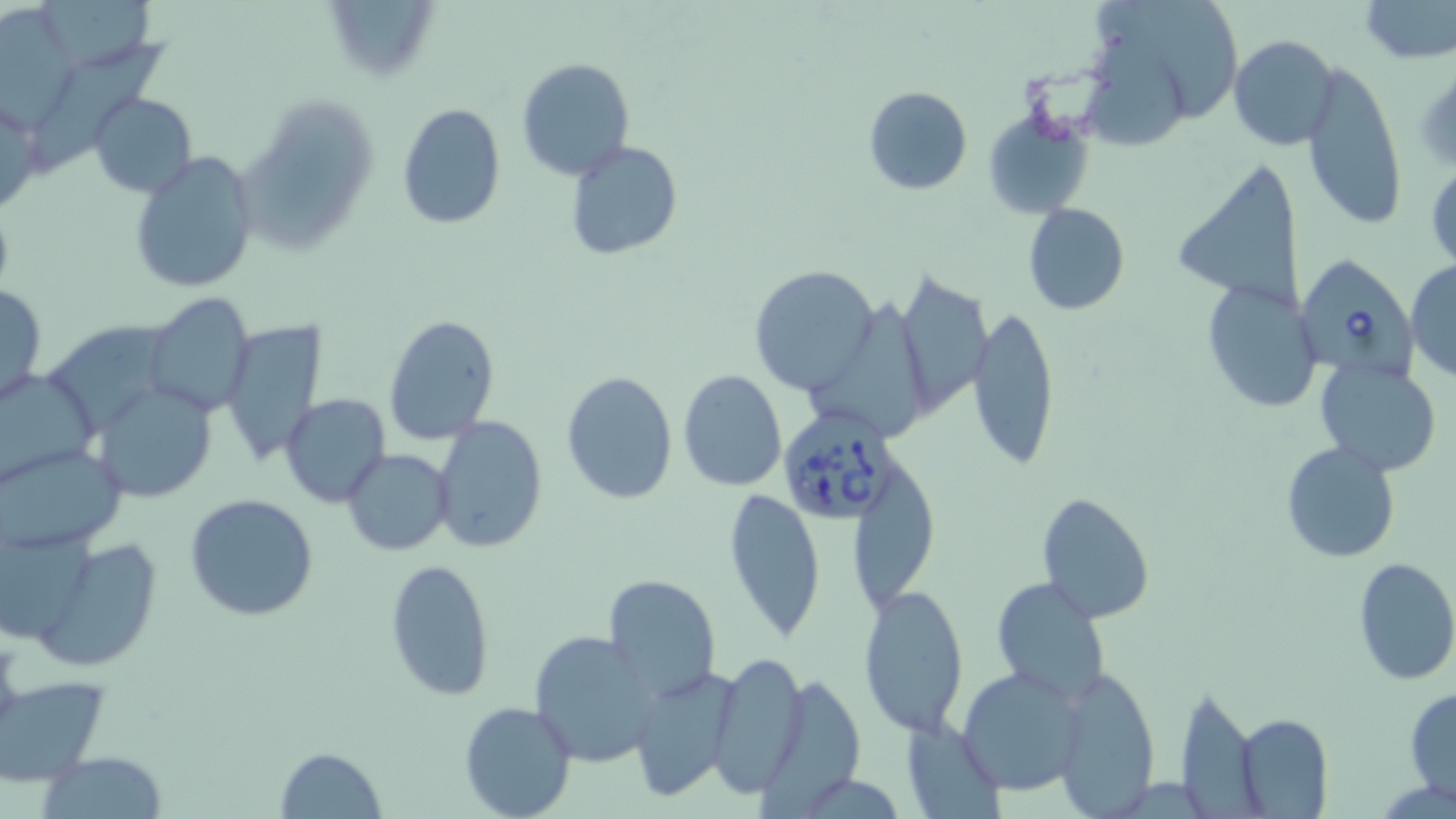

Approximate bounding boxes as [x1, y1, x2, y2] in pixels. Babesia divergens-infected red blood cell locations: [1292, 252, 1419, 381], [778, 406, 898, 522]. Uninfected red blood cell locations: [320, 0, 442, 85], [1358, 0, 1456, 64], [45, 1, 160, 64], [1101, 1, 1244, 118], [0, 8, 76, 130], [1077, 31, 1189, 149], [1229, 34, 1339, 150], [34, 39, 168, 171], [516, 57, 636, 181], [1299, 61, 1408, 230], [1412, 62, 1456, 174], [862, 86, 972, 194], [89, 91, 196, 198], [233, 91, 378, 254], [395, 102, 507, 231], [983, 104, 1096, 222], [565, 140, 682, 260], [129, 149, 259, 294], [1427, 155, 1456, 274], [1170, 163, 1308, 304], [1022, 203, 1131, 315], [1405, 258, 1456, 382], [748, 263, 879, 395], [894, 272, 989, 416], [1201, 280, 1324, 414], [1, 284, 47, 408], [141, 287, 257, 416], [808, 294, 923, 442], [970, 305, 1060, 473], [52, 314, 170, 423], [384, 315, 500, 445], [220, 320, 327, 467], [1315, 359, 1442, 476], [0, 364, 100, 486], [678, 369, 786, 492], [560, 370, 678, 505], [92, 380, 219, 501], [281, 395, 391, 508], [432, 416, 548, 552], [1280, 442, 1401, 565], [2, 443, 126, 555], [343, 449, 453, 555], [854, 462, 940, 617], [723, 487, 826, 641], [1036, 491, 1155, 624], [185, 493, 319, 623], [0, 526, 102, 641], [39, 538, 163, 666], [1351, 557, 1456, 686], [384, 559, 495, 701], [606, 574, 720, 698], [990, 577, 1110, 703], [860, 582, 970, 736], [528, 629, 664, 767], [705, 651, 808, 799], [628, 664, 741, 803], [957, 665, 1088, 795], [1053, 667, 1160, 816], [1, 679, 109, 791], [1404, 687, 1456, 802], [1177, 689, 1266, 819], [459, 701, 578, 819], [1235, 713, 1332, 818], [903, 723, 1003, 817], [275, 746, 386, 819], [38, 751, 167, 818]. Slide-level diagnosis: Babesia divergens. Image is 1456×819 pixels. May-Grünwald-Giemsa stain. Light microscopy. 1000x magnification. One field of a larger specimen. Thin blood smear.